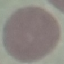
Summary:
  - Malaria status: uninfected
  - Stain: Giemsa
  - Capture: smartphone camera at the microscope eyepiece
  - Preparation: thin blood smear
  - Image type: automatically extracted cell patch, resized to 64 × 64 pixels